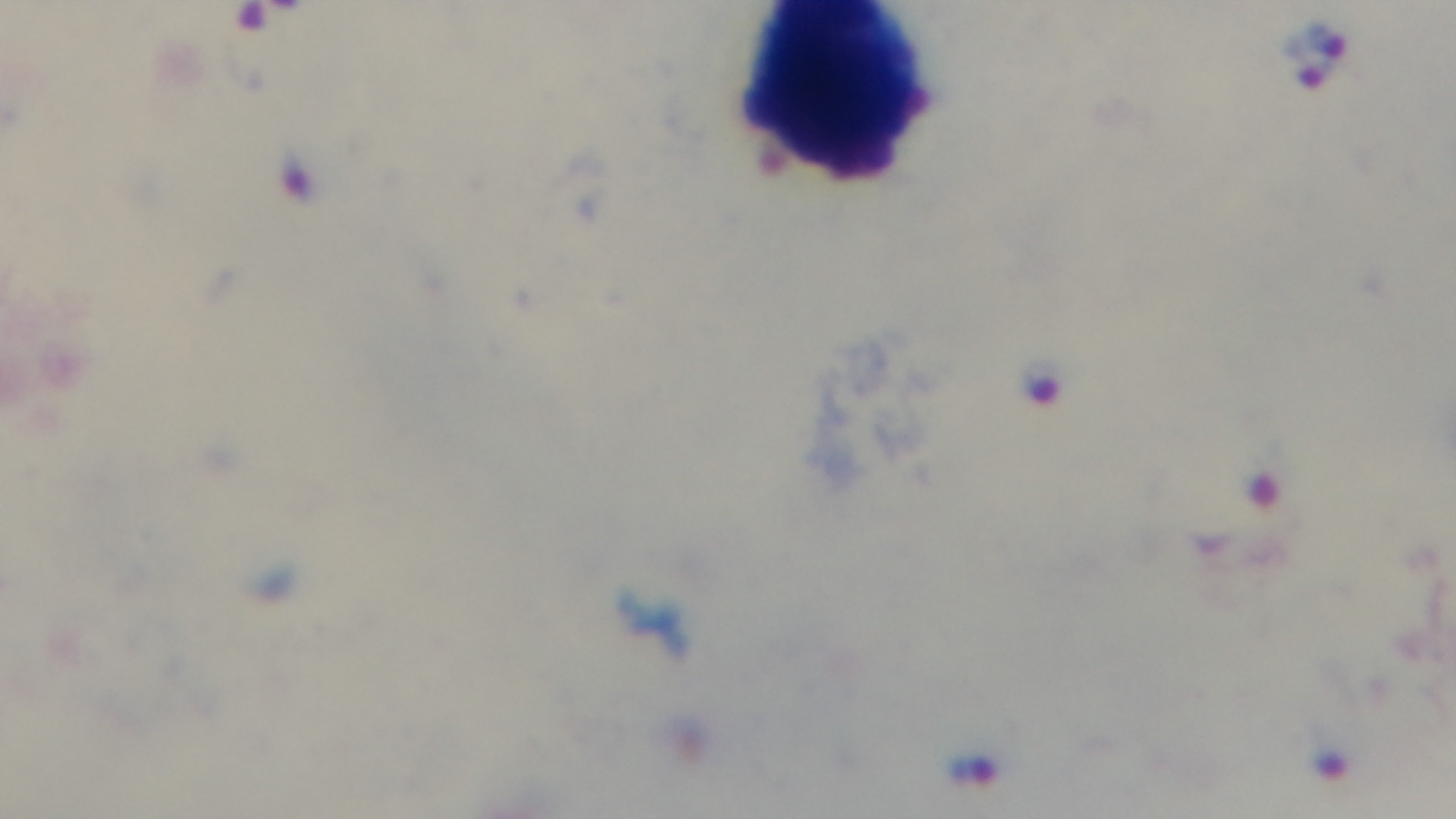

field of view = one from the slide
preparation = thick smear
objective = 100x oil immersion
modality = light microscopy
malaria status = infected
stain = Giemsa
capture = mounted 4K digital camera